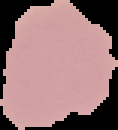
Image is 118×130 pixels. From a thin blood film. Result: negative for Plasmodium parasites. Cell region segmented out of the field of view; the surrounding area is masked to black.